Look for parasitized red blood cells.
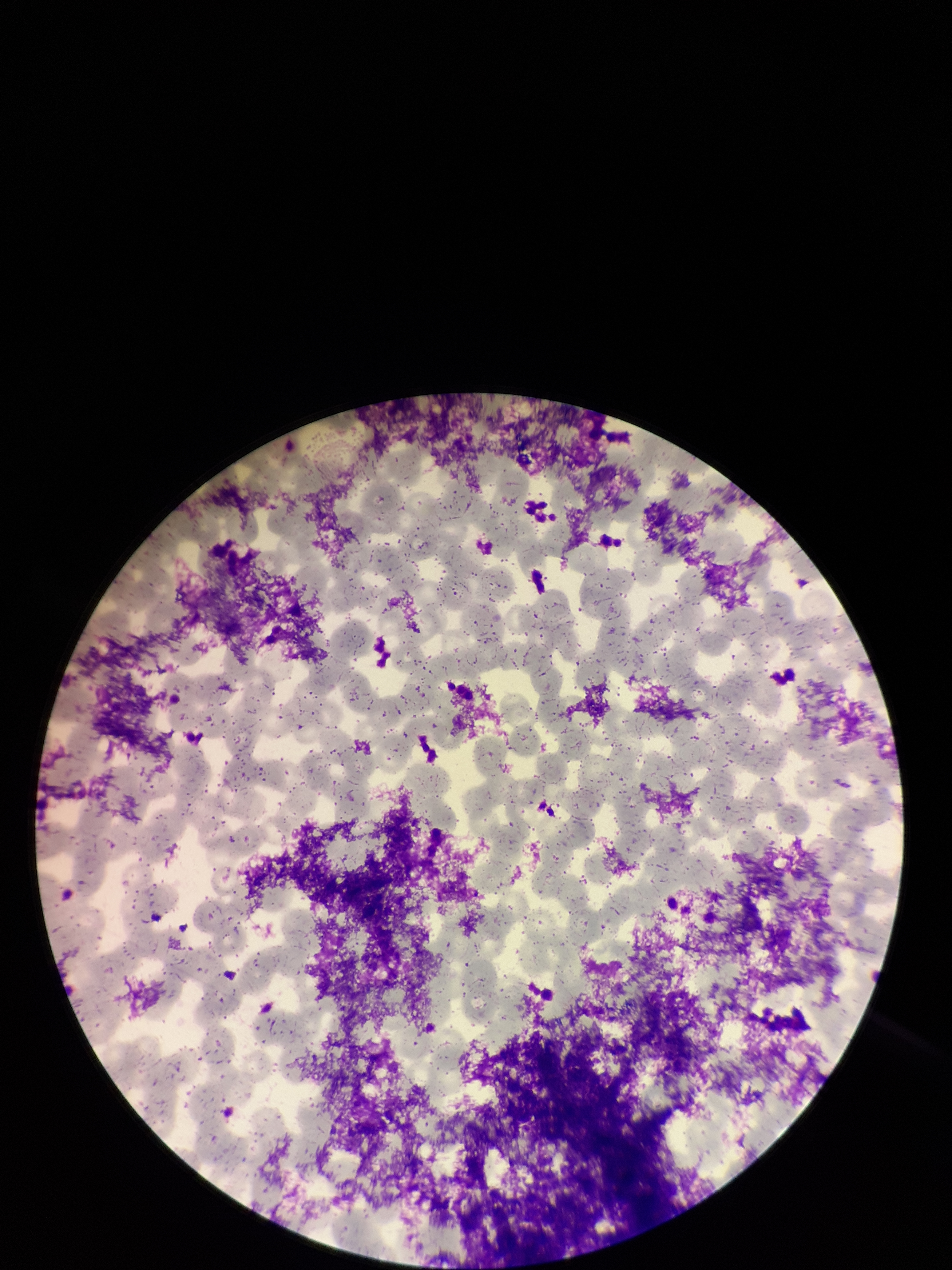
None identified.

Red blood cell count: 306. Smartphone photograph taken through the eyepiece of a microscope. Single field of view. Stained with Giemsa. Image is 952×1270 pixels. Parasitized red blood cell count: 0. Preparation: thin. Patient malaria status: negative.